Outline each blood parasite and name the species.
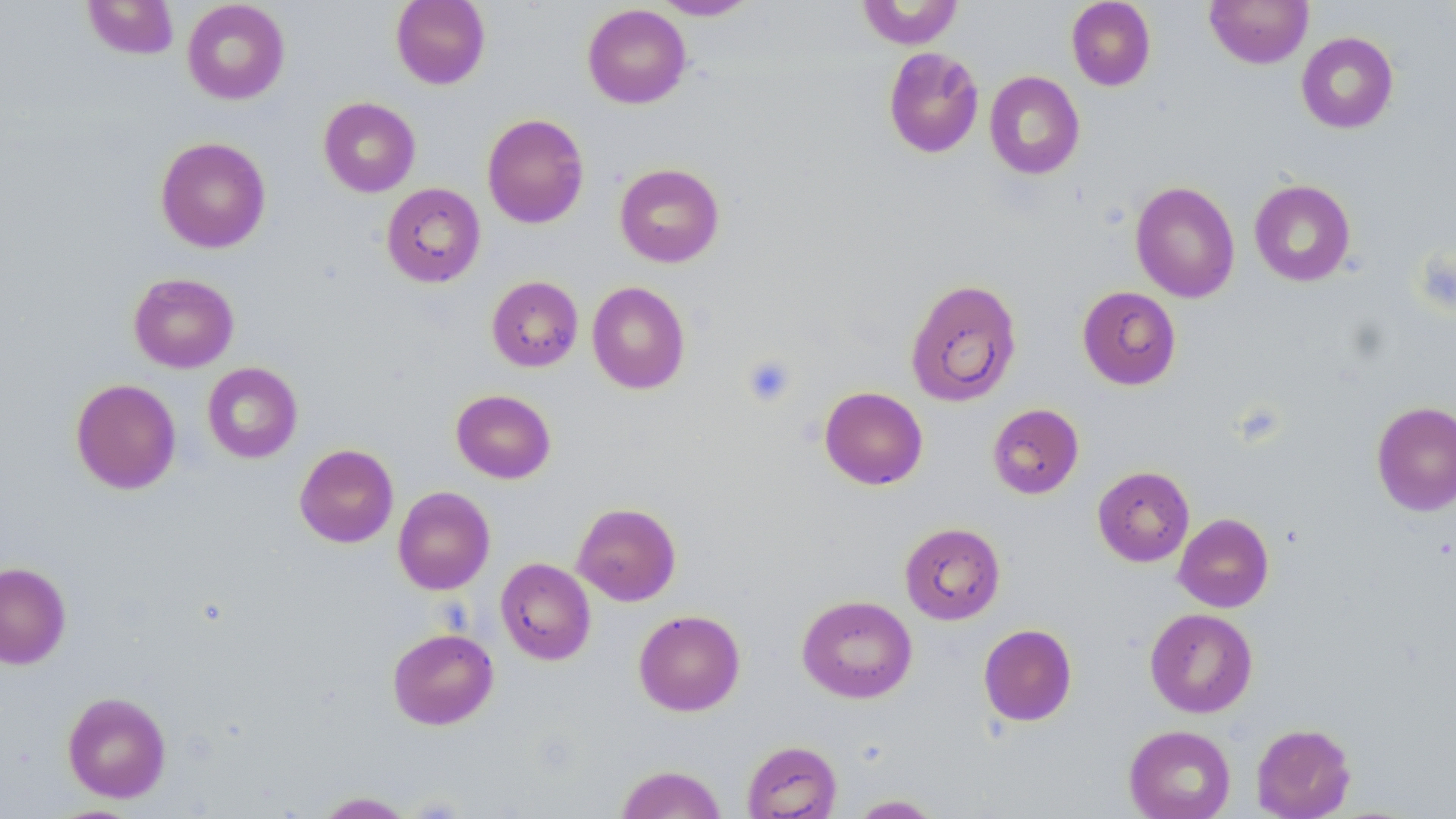
No blood parasites seen.

Summary:
  - Coordinate format: approximate bounding boxes as named x1/y1/x2/y2 corners in pixels
  - Platelet locations: (x1=742, y1=355, x2=796, y2=407)
  - Uninfected red blood cell locations: (x1=82, y1=0, x2=179, y2=60), (x1=182, y1=0, x2=290, y2=105), (x1=390, y1=0, x2=491, y2=89), (x1=651, y1=0, x2=759, y2=20), (x1=1066, y1=0, x2=1156, y2=91), (x1=1205, y1=0, x2=1313, y2=68), (x1=855, y1=1, x2=964, y2=49), (x1=582, y1=4, x2=691, y2=108), (x1=1297, y1=31, x2=1399, y2=133), (x1=882, y1=47, x2=985, y2=159), (x1=984, y1=71, x2=1084, y2=179), (x1=318, y1=97, x2=420, y2=197), (x1=482, y1=113, x2=590, y2=229), (x1=155, y1=136, x2=271, y2=253), (x1=614, y1=163, x2=725, y2=268), (x1=1249, y1=179, x2=1356, y2=286), (x1=1130, y1=180, x2=1240, y2=303), (x1=381, y1=183, x2=485, y2=287), (x1=128, y1=272, x2=239, y2=373), (x1=486, y1=276, x2=583, y2=372), (x1=905, y1=278, x2=1021, y2=407), (x1=587, y1=281, x2=690, y2=394), (x1=1077, y1=286, x2=1181, y2=390), (x1=202, y1=362, x2=303, y2=463), (x1=71, y1=378, x2=181, y2=494), (x1=819, y1=387, x2=928, y2=489), (x1=451, y1=389, x2=556, y2=484), (x1=1371, y1=400, x2=1456, y2=516), (x1=987, y1=403, x2=1084, y2=499), (x1=294, y1=443, x2=398, y2=548), (x1=1092, y1=465, x2=1194, y2=566), (x1=393, y1=486, x2=495, y2=595), (x1=572, y1=502, x2=681, y2=606), (x1=1173, y1=513, x2=1274, y2=612), (x1=899, y1=522, x2=1005, y2=624), (x1=496, y1=557, x2=596, y2=665), (x1=0, y1=561, x2=71, y2=669), (x1=797, y1=594, x2=917, y2=703), (x1=1144, y1=608, x2=1257, y2=717), (x1=634, y1=609, x2=745, y2=715), (x1=978, y1=624, x2=1077, y2=726), (x1=387, y1=628, x2=499, y2=729), (x1=62, y1=691, x2=171, y2=802), (x1=1251, y1=723, x2=1356, y2=818), (x1=1124, y1=725, x2=1236, y2=819), (x1=741, y1=740, x2=842, y2=818), (x1=616, y1=764, x2=727, y2=818), (x1=313, y1=791, x2=416, y2=818), (x1=850, y1=794, x2=942, y2=818)
  - Slide-level diagnosis: no evidence of blood parasites
  - Modality: light microscopy
  - Magnification: 1000x
  - Image size: 1456×819 pixels
  - Field of view: one of a larger specimen
  - Stain: May-Grünwald-Giemsa
  - Preparation: thin blood film